Classify this cell by malaria status.
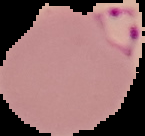
Parasitized.

Summary:
  - Image size: 145×136 pixels
  - Preparation: thin blood film
  - Image type: segmented cell region on a black background